Report the malaria status of this cell.
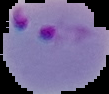
Parasitized.

Cell region segmented out of the field of view; the surrounding area is masked to black. From a thin blood smear. Image is 109×94 pixels.